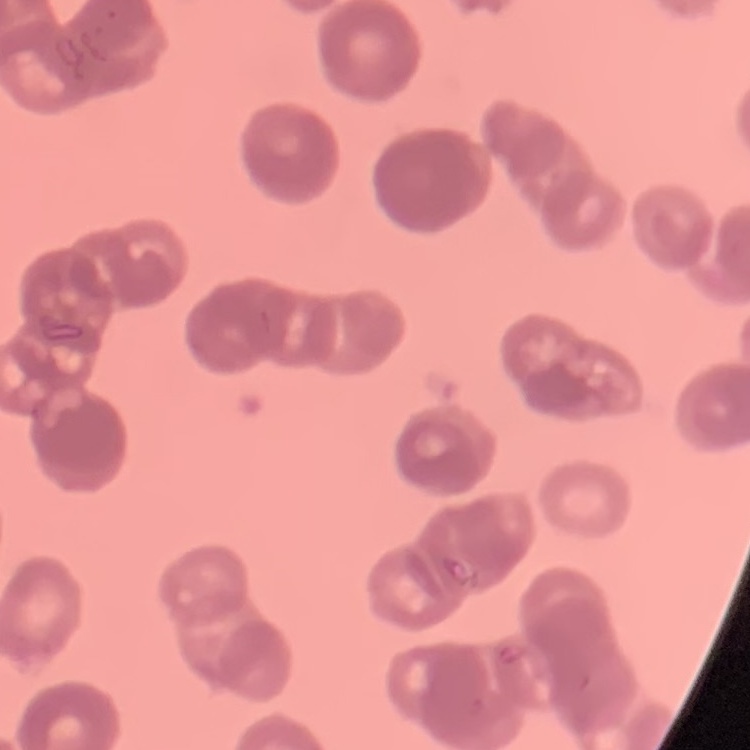

Summary:
  - Red blood cell morphology: rouleaux formation
  - Preparation: thin blood film
  - Image type: square crop of a larger photomicrograph
  - Stain: Field's or Giemsa